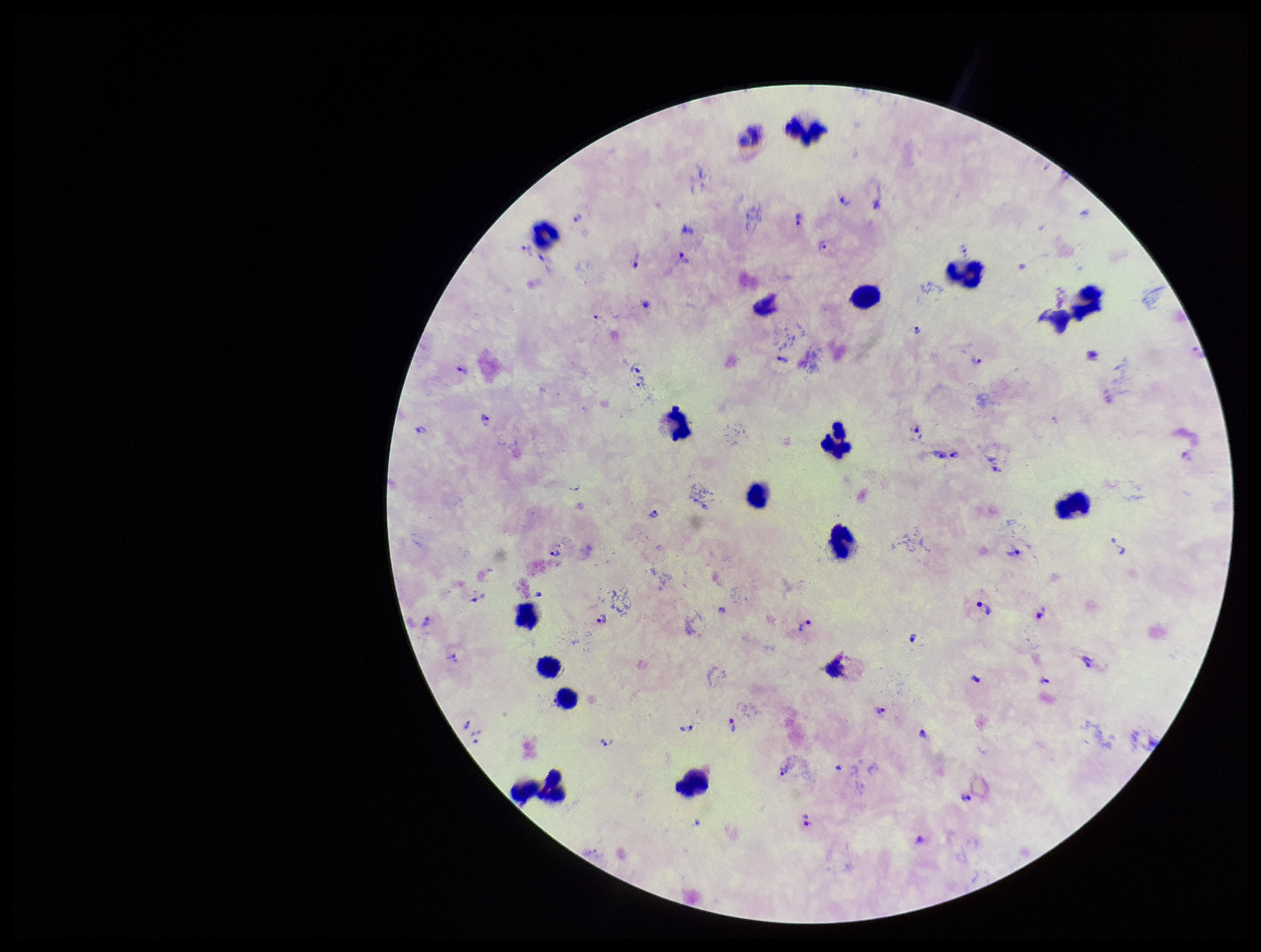

Plasmodium parasites: detected. Image is 1261×952 pixels. Leukocyte count: 19. Photographed through the microscope eyepiece with a smartphone camera. One field from this slide. Giemsa stain. Preparation: thick. Species reported for this patient: Plasmodium vivax. Parasite count: 42. Patient malaria status: infected.